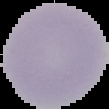
Summary:
  - Preparation: thin blood smear
  - Result: negative for malaria parasites
  - Image type: segmented cell region on a black background
  - Image size: 109×109 pixels